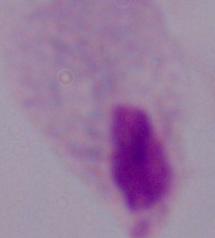

A trichomonad is seen. Micrograph. Captured at 1000x magnification.